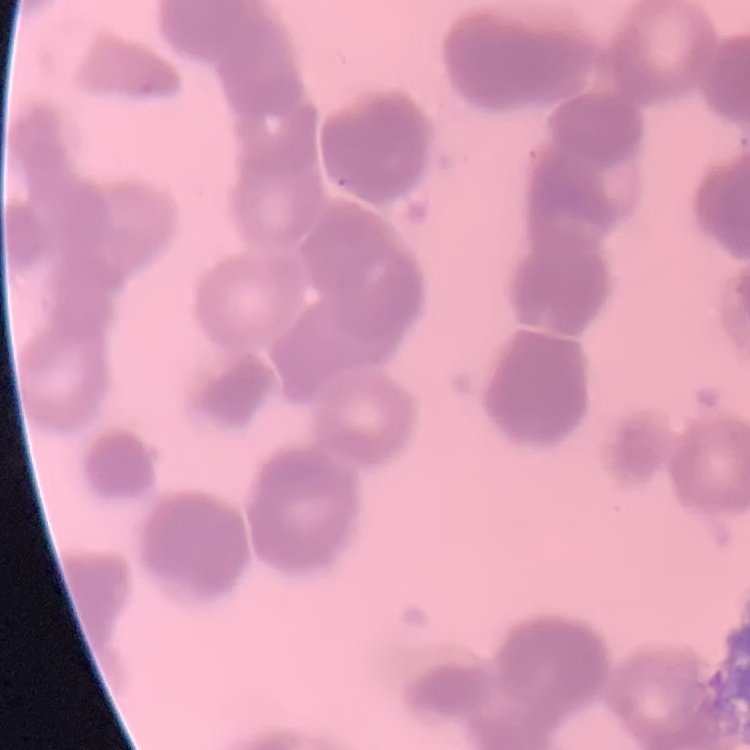 The erythrocytes show rouleaux formation. Stained with either Field's or Giemsa. Thin blood smear. One tile cut from a larger photomicrograph.